Look for Plasmodium parasites.
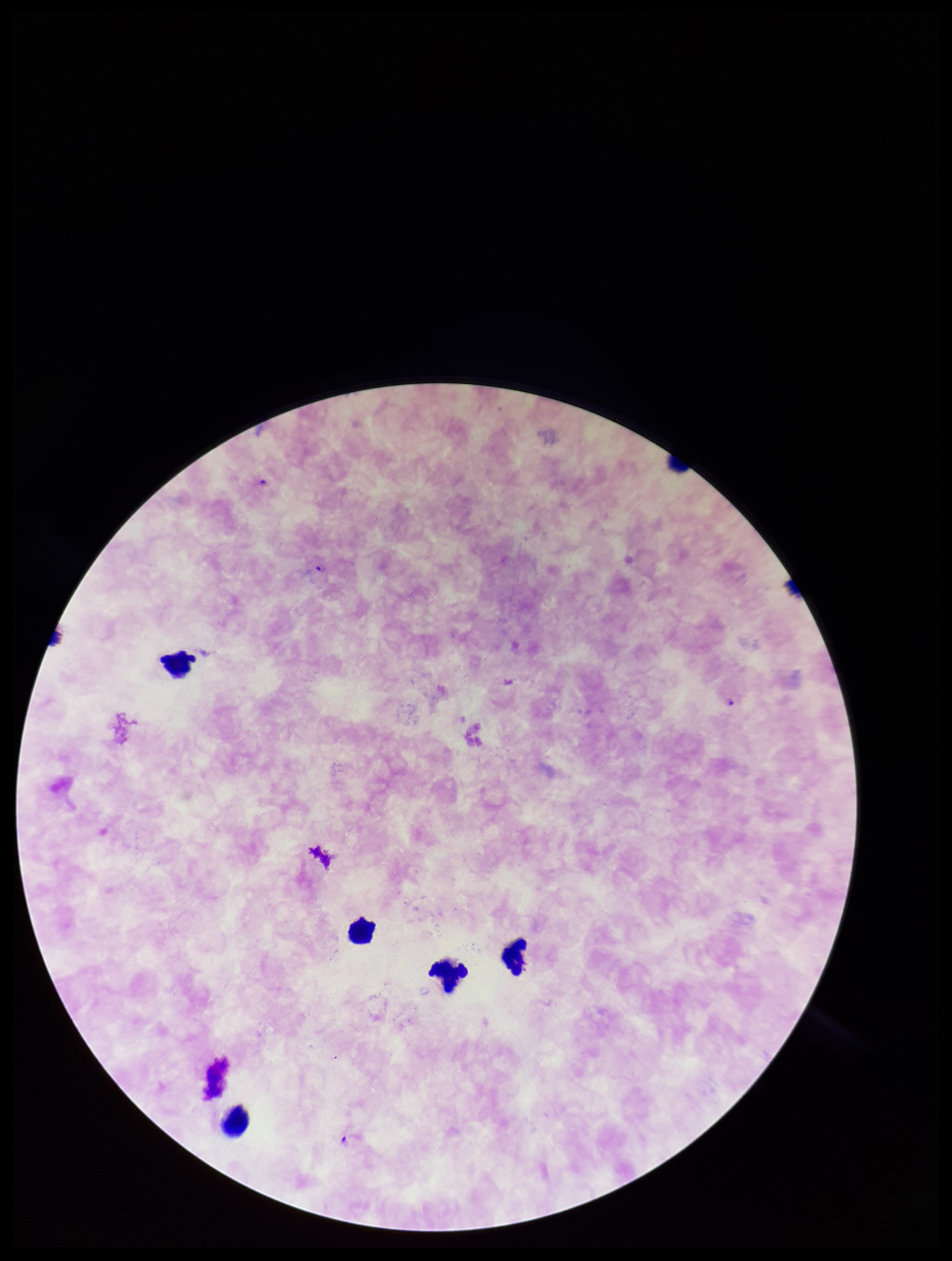

Identified.

Giemsa stain. Patient malaria status: infected. Single field of view. Species reported for this patient: Plasmodium falciparum. Photographed through the microscope eyepiece with a smartphone camera. Preparation: thick smear. Image is 952×1261 pixels. Leukocyte count: 5. Parasite count: 4.